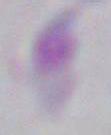

Summary:
  - Identification: Toxoplasma gondii
  - Magnification: 1000x
  - Modality: photomicrograph